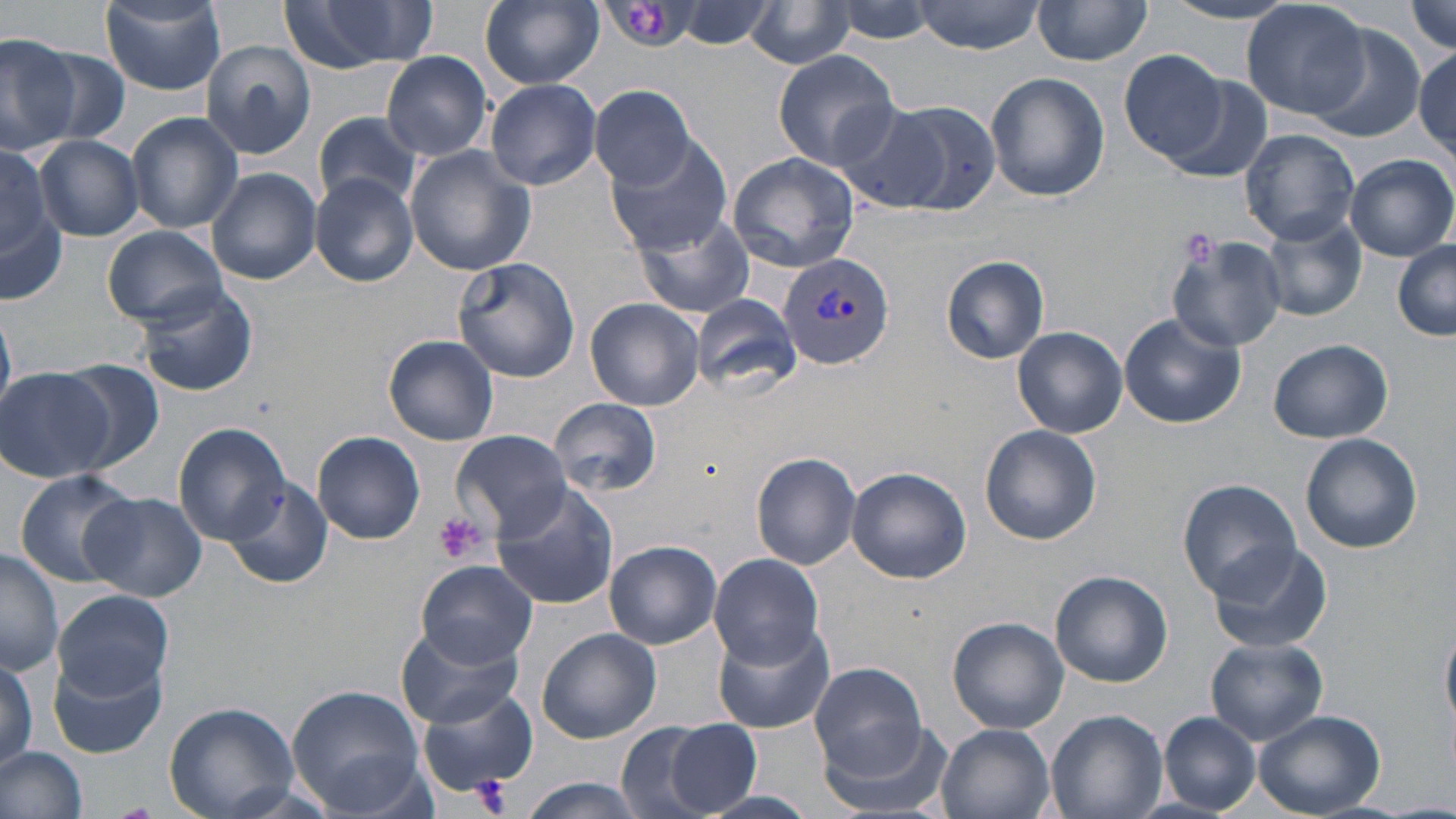
Summary:
  - Coordinate format: approximate bounding boxes as (x1,y1)-(x2,y2) corner pairs in pixels
  - Plasmodium vivax-infected red blood cell locations: (777,252)-(895,370)
  - Platelet locations: (625,1)-(668,44), (1183,234)-(1217,267), (433,511)-(489,565), (471,774)-(513,816)
  - Uninfected red blood cell locations: (277,0)-(440,75), (480,0)-(604,89), (830,0)-(937,48), (915,0)-(1044,54), (1241,0)-(1371,120), (674,1)-(776,49), (1033,1)-(1152,67), (100,2)-(225,93), (1161,2)-(1301,23), (1407,2)-(1455,54), (745,4)-(854,69), (1307,30)-(1421,144), (0,34)-(80,152), (202,40)-(317,159), (1121,48)-(1228,163), (1413,48)-(1455,154), (771,50)-(900,171), (380,51)-(493,162), (984,71)-(1110,202), (1155,71)-(1274,181), (484,78)-(601,190), (589,84)-(697,189), (833,100)-(953,213), (883,101)-(1000,216), (126,111)-(244,236), (313,113)-(425,209), (1240,128)-(1360,245), (605,135)-(732,256), (34,136)-(143,240), (0,145)-(59,268), (404,146)-(537,276), (726,152)-(860,272), (1346,153)-(1455,261), (207,169)-(321,285), (310,174)-(418,288), (632,210)-(757,320), (1259,214)-(1367,323), (4,217)-(67,307), (102,225)-(229,327), (1166,233)-(1289,351), (1393,239)-(1456,341), (941,255)-(1050,363), (451,257)-(582,382), (133,281)-(261,397), (690,293)-(802,394), (585,295)-(705,412), (1118,313)-(1246,428), (1012,326)-(1128,438), (383,335)-(500,446), (1269,339)-(1393,443), (55,361)-(168,472), (1,368)-(117,483), (550,398)-(661,496), (173,423)-(291,543), (981,425)-(1102,545), (452,429)-(572,540), (313,431)-(427,544), (1299,431)-(1423,553), (751,451)-(862,569), (846,466)-(971,584), (13,469)-(142,586), (223,475)-(333,589), (1179,478)-(1301,598), (491,483)-(621,609), (81,491)-(208,602), (604,539)-(721,649), (1206,539)-(1335,654), (1,548)-(63,674), (709,552)-(825,667), (417,560)-(537,666), (1050,570)-(1173,687), (53,588)-(175,700), (948,616)-(1069,733), (713,617)-(833,733), (398,619)-(526,729), (1442,627)-(1456,736), (538,628)-(661,744), (1206,638)-(1327,745), (0,654)-(37,774), (49,655)-(166,760), (809,661)-(927,776), (287,684)-(426,815), (417,687)-(541,798), (163,701)-(299,819), (1043,709)-(1167,819), (1255,710)-(1383,816), (1158,711)-(1263,815), (813,715)-(951,819), (657,720)-(763,816), (614,723)-(728,819), (935,724)-(1056,819), (0,746)-(90,819), (516,777)-(652,818)
  - Slide-level diagnosis: Plasmodium vivax
  - Field of view: single
  - Magnification: 1000x
  - Modality: optical microscopy
  - Image size: 1456×819 pixels
  - Stain: May-Grünwald-Giemsa
  - Preparation: thin blood smear